Comment on the morphology of the erythrocytes.
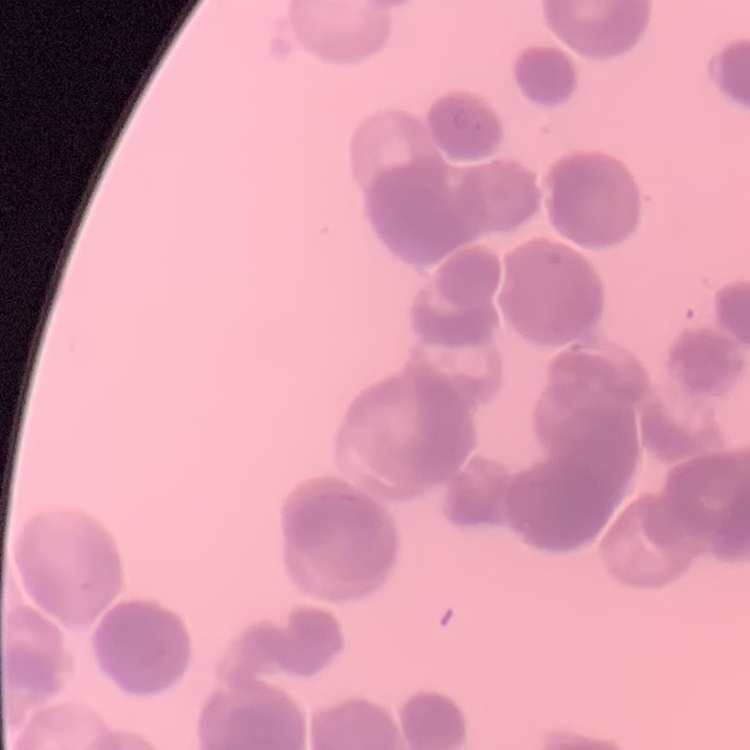
Rouleaux formation.

Summary:
  - Image type: square crop of a larger photomicrograph
  - Stain: Field's or Giemsa
  - Preparation: thin blood film